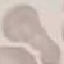

malaria status = uninfected
preparation = thin blood film
image type = automatically extracted cell patch, resized to 64 × 64 pixels
capture = smartphone through the microscope eyepiece
stain = Giemsa